Assess this cell for malaria.
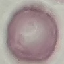

Uninfected.

image type = cell patch, automatically extracted from a larger field of view and resized to 64 × 64 pixels
stain = Giemsa
preparation = thin blood smear
capture = smartphone through the microscope eyepiece